Point out every malaria parasite.
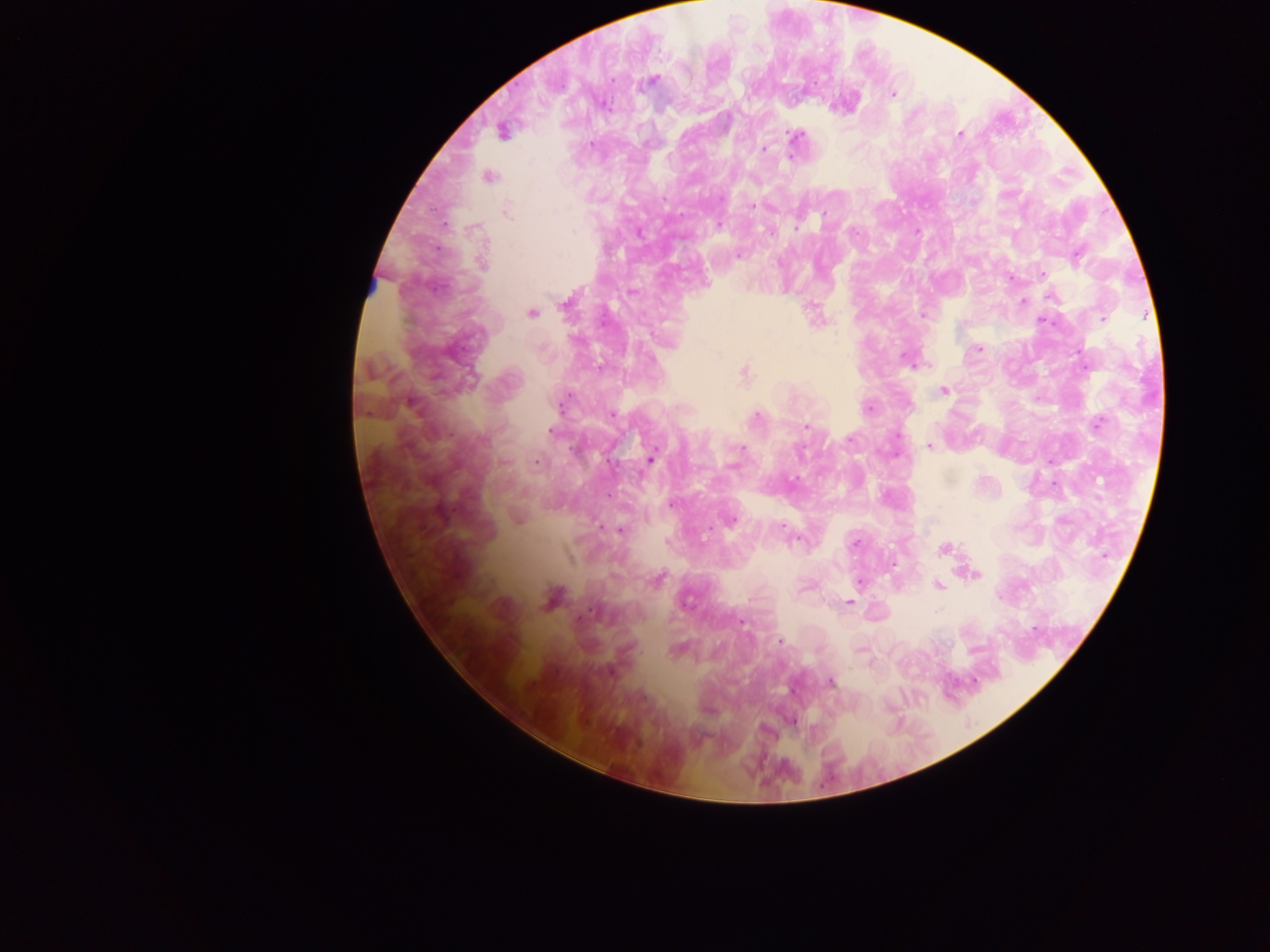

Approximate centers as {x, y} in pixels.
Malaria parasites: {650, 81}, {892, 93}, {502, 130}, {960, 133}, {794, 137}, {764, 149}, {488, 176}, {752, 205}, {507, 211}, {718, 224}, {916, 232}, {738, 255}, {1041, 274}, {631, 292}, {1051, 296}, {1022, 300}, {531, 313}, {924, 314}, {1103, 318}, {978, 348}, {913, 362}, {600, 368}, {743, 374}, {942, 391}, {564, 402}, {868, 407}, {612, 414}, {756, 417}, {1097, 423}, {806, 426}, {552, 431}, {929, 445}, {741, 448}, {650, 459}, {536, 461}, {1050, 462}, {672, 502}, {518, 516}, {729, 519}, {783, 527}, {620, 530}, {855, 543}, {943, 549}, {970, 574}, {657, 579}, {859, 581}, {939, 585}, {551, 598}, {849, 602}, {741, 622}, {780, 641}, {859, 647}, {676, 649}, {830, 681}, {792, 720}.

Summary:
  - Leukocyte locations: {370, 288}
  - Image size: 1270×952 pixels
  - Country: Ghana
  - Capture: mobile-phone photograph through a microscope
  - Preparation: thick blood film
  - Field of view: single